State the blood parasite species.
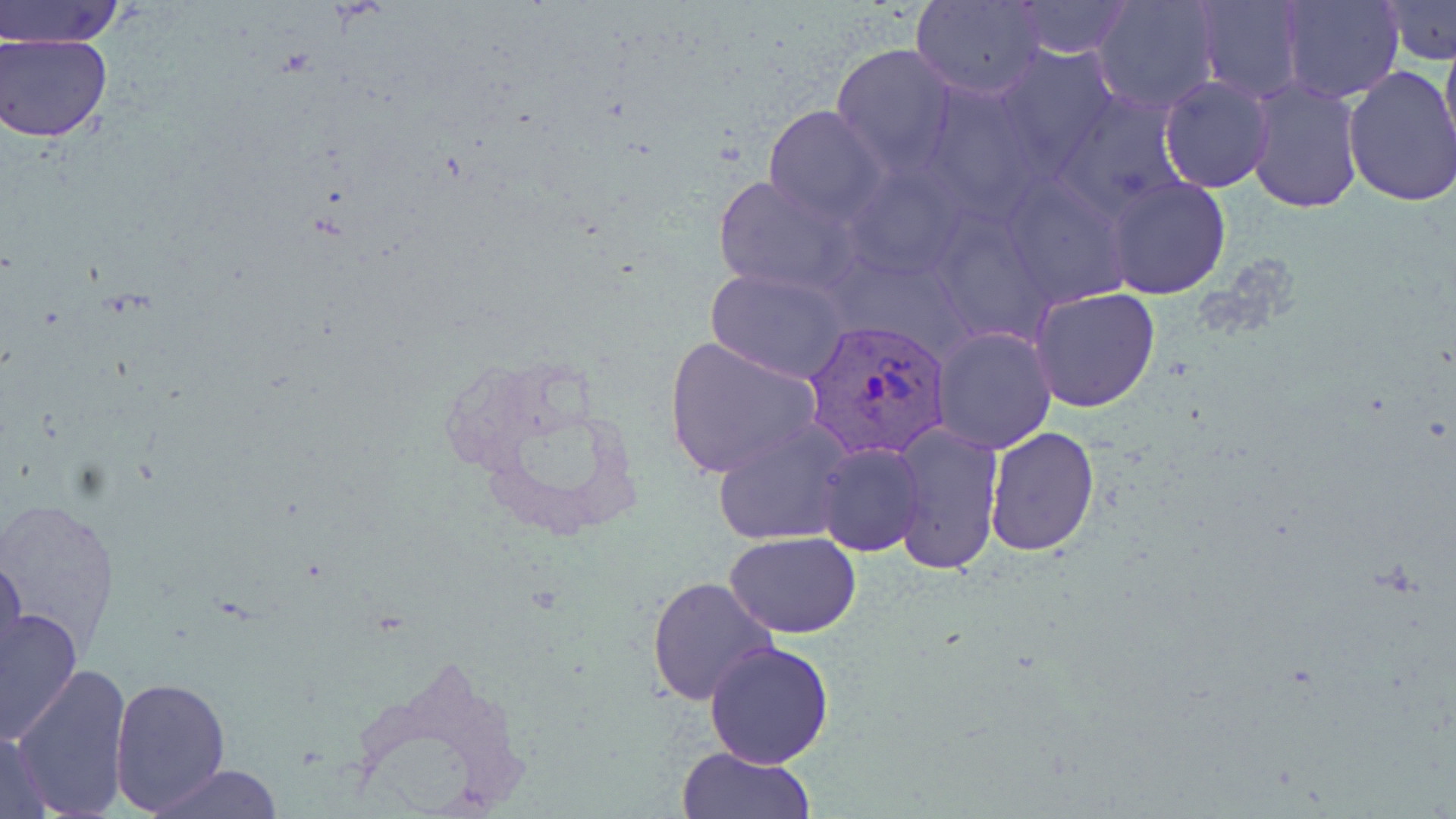

Plasmodium vivax.

Approximate bounding boxes as (x1,y1)-(x2,y2) corner pairs in pixels. Uninfected red blood cell locations: (3,0)-(124,47), (1092,0)-(1219,114), (1195,0)-(1306,101), (1280,0)-(1403,102), (911,1)-(1045,99), (1013,1)-(1131,57), (1380,1)-(1456,65), (1439,31)-(1456,160), (2,33)-(116,142), (832,43)-(959,174), (993,45)-(1121,179), (1342,64)-(1456,208), (1158,75)-(1276,194), (1245,77)-(1363,213), (917,80)-(1045,219), (1054,88)-(1189,220), (763,104)-(889,225), (843,160)-(972,281), (713,172)-(861,297), (1000,172)-(1135,311), (1106,175)-(1231,298), (927,205)-(1055,343), (706,269)-(849,382), (1030,287)-(1160,413), (930,325)-(1057,453), (663,335)-(821,478), (713,419)-(853,546), (888,421)-(1005,576), (984,425)-(1101,556), (816,442)-(924,556), (725,534)-(862,637), (0,553)-(27,681), (647,574)-(777,707), (0,605)-(83,743), (704,642)-(834,769), (13,662)-(132,819), (111,675)-(230,812), (0,729)-(53,818), (678,745)-(813,819), (152,766)-(284,819). Plasmodium vivax-infected red blood cell locations: (802,315)-(952,461). Captured at 1000x magnification. Image is 1456×819 pixels. May-Grünwald-Giemsa stain. One field of a larger specimen. Light microscopy. Thin blood film.